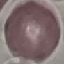
Malaria status: uninfected. Giemsa stain. Thin blood smear. Photographed with a smartphone camera at the microscope eyepiece. Cell patch, automatically extracted from a larger field of view and resized to 64 × 64 pixels.